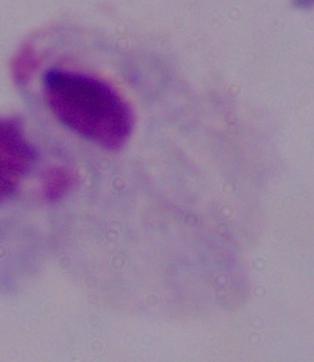

1000x magnification. A trichomonad is shown. Photomicrograph.